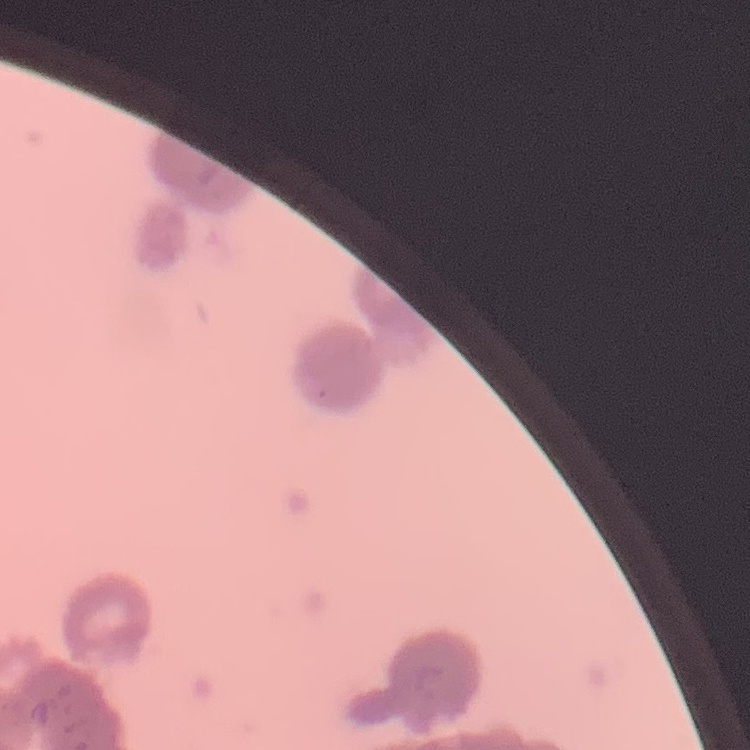

Summary:
  - Red blood cell morphology: rouleaux formation
  - Stain: Field's or Giemsa
  - Preparation: thin blood film
  - Image type: one tile cut from a larger photomicrograph